Describe the morphology of the erythrocytes.
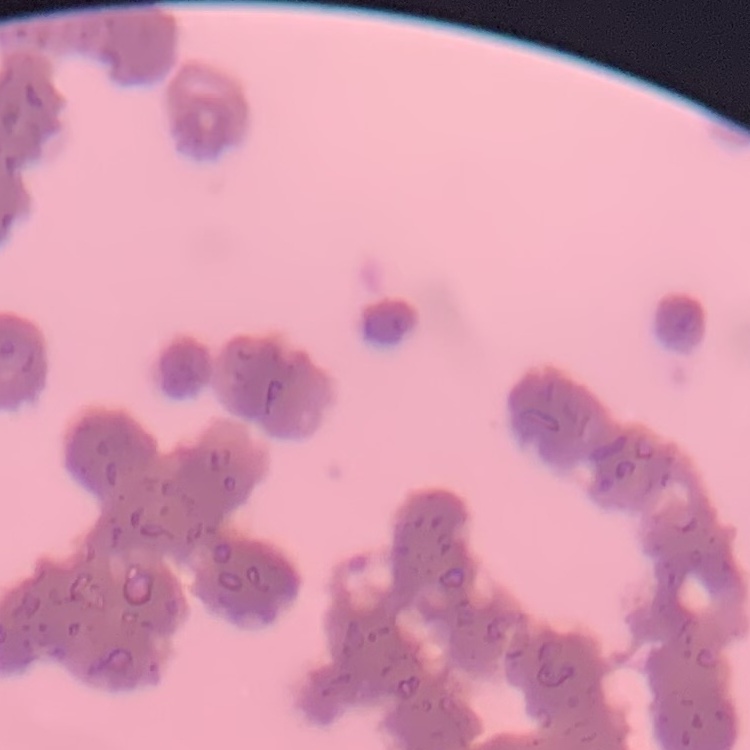
They show rouleaux formation.

preparation = thin blood film
stain = Field's or Giemsa
image type = square crop of a larger photomicrograph